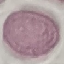
Summary:
  - Result: no malaria parasites seen
  - Preparation: thin blood film
  - Image type: cell patch, automatically extracted from a larger field of view and resized to 64 × 64 pixels
  - Stain: Giemsa
  - Capture: smartphone through the microscope eyepiece